Assess this cell for malaria.
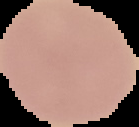
Uninfected.

The area outside the segmented cell region is set to black. From a thin blood film. Image is 139×127 pixels.